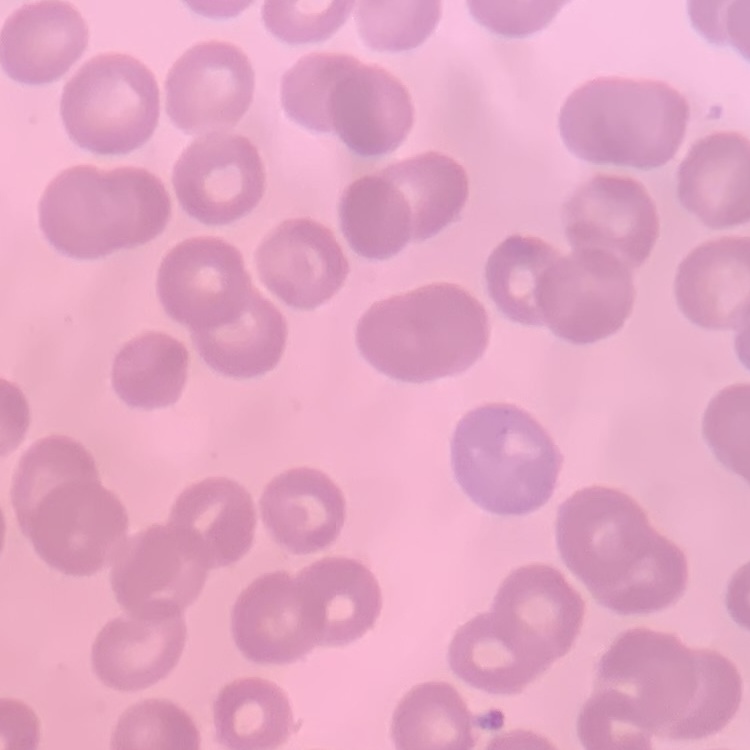

Summary:
  - Red blood cell morphology: no rouleaux formation
  - Stain: Field's or Giemsa
  - Preparation: thin blood smear
  - Image type: square crop of a larger photomicrograph